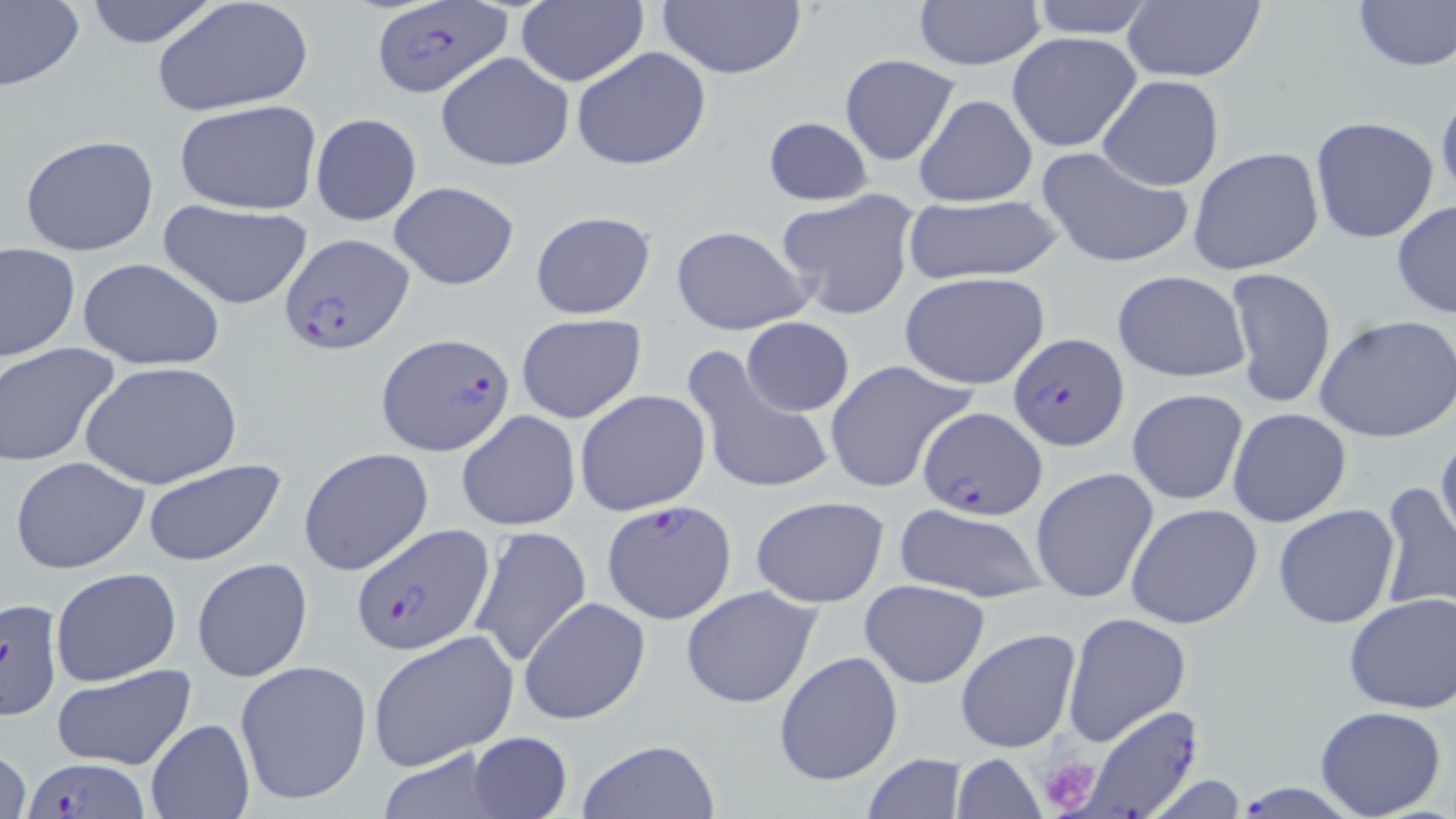

Approximate bounding boxes as named x1/y1/x2/y2 corners in pixels. Plasmodium falciparum-infected red blood cell locations: (x1=370, y1=3, x2=510, y2=100), (x1=283, y1=232, x2=413, y2=355), (x1=376, y1=332, x2=515, y2=458), (x1=1008, y1=333, x2=1129, y2=451), (x1=916, y1=406, x2=1049, y2=519), (x1=601, y1=501, x2=735, y2=626), (x1=353, y1=523, x2=496, y2=656), (x1=1, y1=596, x2=65, y2=720), (x1=1071, y1=704, x2=1211, y2=817), (x1=25, y1=753, x2=146, y2=818), (x1=1241, y1=774, x2=1341, y2=819). Uninfected red blood cell locations: (x1=0, y1=0, x2=85, y2=92), (x1=81, y1=0, x2=223, y2=49), (x1=151, y1=0, x2=313, y2=119), (x1=514, y1=0, x2=647, y2=87), (x1=656, y1=0, x2=808, y2=80), (x1=910, y1=0, x2=1046, y2=69), (x1=1023, y1=0, x2=1162, y2=40), (x1=1117, y1=0, x2=1269, y2=83), (x1=1351, y1=0, x2=1455, y2=72), (x1=1007, y1=31, x2=1144, y2=153), (x1=570, y1=47, x2=714, y2=170), (x1=435, y1=51, x2=574, y2=172), (x1=839, y1=53, x2=961, y2=167), (x1=1097, y1=75, x2=1225, y2=191), (x1=1435, y1=86, x2=1456, y2=206), (x1=913, y1=93, x2=1038, y2=207), (x1=173, y1=100, x2=321, y2=215), (x1=310, y1=112, x2=422, y2=226), (x1=762, y1=115, x2=873, y2=204), (x1=1309, y1=115, x2=1441, y2=244), (x1=18, y1=134, x2=159, y2=257), (x1=1036, y1=146, x2=1196, y2=271), (x1=1187, y1=146, x2=1324, y2=276), (x1=390, y1=180, x2=520, y2=290), (x1=774, y1=188, x2=922, y2=321), (x1=899, y1=193, x2=1066, y2=288), (x1=159, y1=200, x2=315, y2=311), (x1=1391, y1=200, x2=1456, y2=321), (x1=529, y1=210, x2=657, y2=319), (x1=670, y1=224, x2=815, y2=336), (x1=1, y1=242, x2=79, y2=361), (x1=76, y1=256, x2=225, y2=372), (x1=1225, y1=266, x2=1337, y2=409), (x1=1111, y1=270, x2=1252, y2=383), (x1=899, y1=272, x2=1051, y2=390), (x1=514, y1=313, x2=647, y2=425), (x1=1314, y1=314, x2=1456, y2=443), (x1=741, y1=317, x2=854, y2=418), (x1=0, y1=342, x2=121, y2=467), (x1=684, y1=346, x2=834, y2=495), (x1=823, y1=359, x2=975, y2=494), (x1=80, y1=361, x2=243, y2=489), (x1=575, y1=388, x2=712, y2=516), (x1=1126, y1=388, x2=1249, y2=505), (x1=1226, y1=409, x2=1352, y2=528), (x1=456, y1=410, x2=581, y2=531), (x1=1435, y1=429, x2=1456, y2=553), (x1=298, y1=447, x2=434, y2=577), (x1=9, y1=455, x2=150, y2=573), (x1=140, y1=458, x2=286, y2=568), (x1=1030, y1=467, x2=1159, y2=606), (x1=1376, y1=481, x2=1456, y2=615), (x1=749, y1=495, x2=891, y2=608), (x1=891, y1=501, x2=1051, y2=604), (x1=1125, y1=503, x2=1263, y2=629), (x1=1273, y1=504, x2=1401, y2=629), (x1=467, y1=526, x2=592, y2=667), (x1=191, y1=557, x2=313, y2=684), (x1=49, y1=567, x2=181, y2=686), (x1=859, y1=579, x2=988, y2=688), (x1=680, y1=585, x2=822, y2=709), (x1=1340, y1=593, x2=1456, y2=713), (x1=519, y1=597, x2=651, y2=725), (x1=1061, y1=613, x2=1191, y2=746), (x1=956, y1=628, x2=1080, y2=754), (x1=365, y1=629, x2=518, y2=770), (x1=774, y1=650, x2=904, y2=787), (x1=233, y1=659, x2=372, y2=806), (x1=52, y1=664, x2=196, y2=771), (x1=1315, y1=705, x2=1447, y2=819), (x1=146, y1=719, x2=253, y2=818), (x1=465, y1=731, x2=574, y2=818), (x1=575, y1=738, x2=720, y2=818), (x1=0, y1=743, x2=30, y2=819), (x1=372, y1=745, x2=515, y2=819), (x1=948, y1=753, x2=1046, y2=819), (x1=859, y1=754, x2=973, y2=819). Platelet locations: (x1=1037, y1=756, x2=1103, y2=817). Slide-level diagnosis: Plasmodium falciparum. Optical microscopy. May-Grünwald-Giemsa stain. Image is 1456×819 pixels. Thin blood film. One field of a larger specimen. 1000x magnification.